Outline platelets.
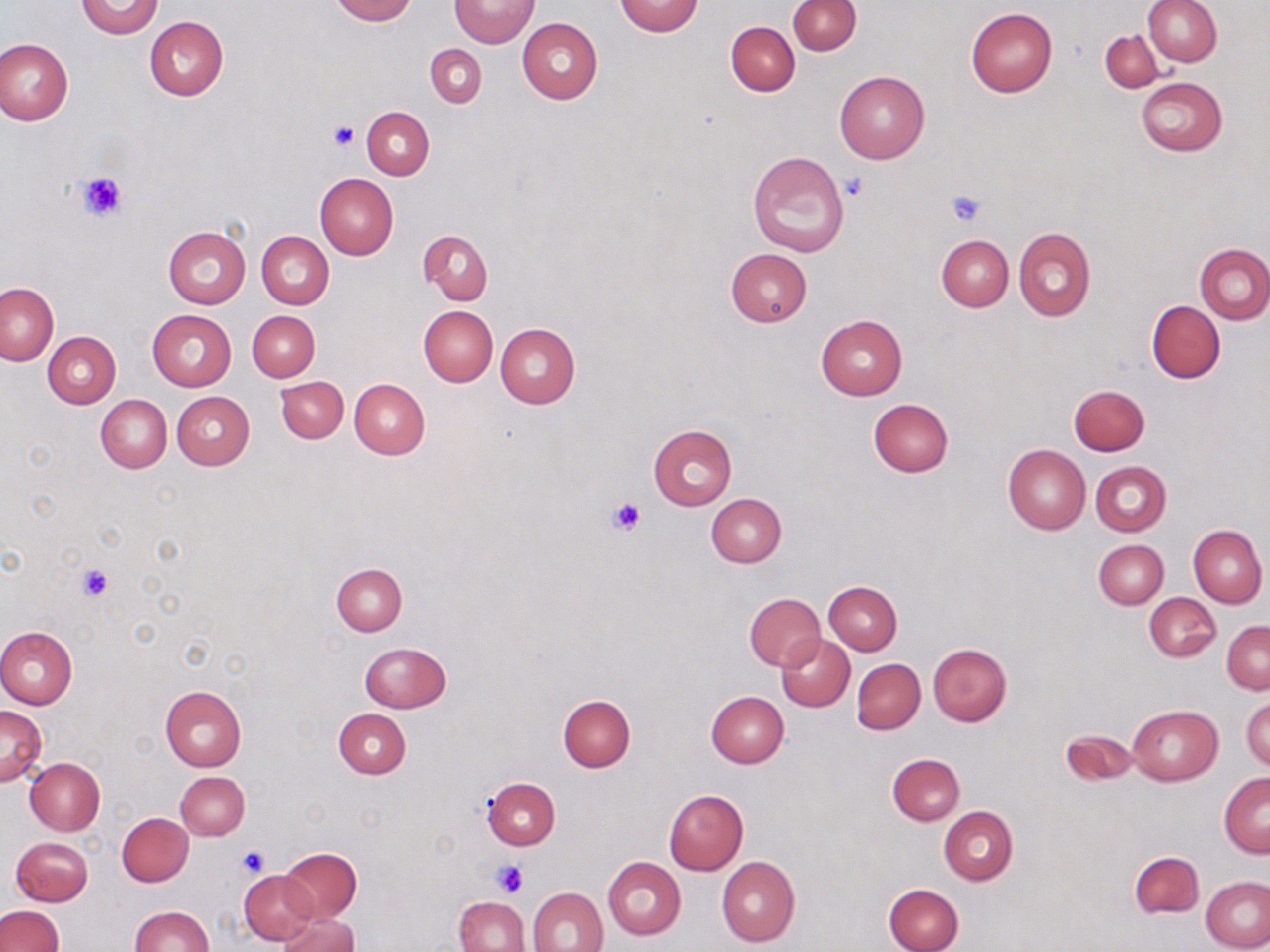
Approximate bounding boxes as named x1/y1/x2/y2 corners in pixels.
Platelets: (x1=329, y1=121, x2=359, y2=151), (x1=75, y1=170, x2=129, y2=222), (x1=842, y1=172, x2=868, y2=201), (x1=945, y1=189, x2=987, y2=226), (x1=609, y1=498, x2=646, y2=535), (x1=75, y1=564, x2=114, y2=601), (x1=234, y1=843, x2=271, y2=878), (x1=490, y1=859, x2=526, y2=898).

Uninfected red blood cell locations: (x1=77, y1=0, x2=163, y2=38), (x1=329, y1=0, x2=417, y2=23), (x1=450, y1=0, x2=538, y2=48), (x1=1143, y1=0, x2=1222, y2=66), (x1=614, y1=1, x2=704, y2=36), (x1=787, y1=1, x2=860, y2=55), (x1=966, y1=8, x2=1058, y2=97), (x1=145, y1=16, x2=228, y2=100), (x1=517, y1=17, x2=603, y2=103), (x1=726, y1=22, x2=799, y2=95), (x1=1100, y1=31, x2=1163, y2=91), (x1=0, y1=38, x2=72, y2=127), (x1=426, y1=44, x2=486, y2=108), (x1=834, y1=70, x2=930, y2=163), (x1=1136, y1=76, x2=1228, y2=156), (x1=361, y1=106, x2=434, y2=180), (x1=746, y1=150, x2=849, y2=256), (x1=315, y1=173, x2=399, y2=259), (x1=163, y1=226, x2=251, y2=309), (x1=1013, y1=227, x2=1095, y2=322), (x1=418, y1=230, x2=493, y2=304), (x1=257, y1=231, x2=334, y2=309), (x1=937, y1=236, x2=1013, y2=311), (x1=1196, y1=243, x2=1270, y2=324), (x1=725, y1=248, x2=811, y2=327), (x1=1169, y1=254, x2=1264, y2=358), (x1=0, y1=282, x2=59, y2=366), (x1=1146, y1=300, x2=1225, y2=383), (x1=418, y1=306, x2=496, y2=386), (x1=147, y1=310, x2=235, y2=392), (x1=247, y1=311, x2=319, y2=380), (x1=816, y1=315, x2=907, y2=400), (x1=494, y1=323, x2=579, y2=408), (x1=43, y1=332, x2=120, y2=408), (x1=276, y1=376, x2=348, y2=442), (x1=349, y1=378, x2=430, y2=459), (x1=1069, y1=385, x2=1149, y2=456), (x1=172, y1=392, x2=254, y2=470), (x1=96, y1=395, x2=171, y2=472), (x1=867, y1=398, x2=954, y2=477), (x1=647, y1=424, x2=738, y2=510), (x1=1003, y1=443, x2=1090, y2=534), (x1=1092, y1=461, x2=1171, y2=536), (x1=706, y1=494, x2=786, y2=567), (x1=1188, y1=525, x2=1267, y2=608), (x1=1093, y1=539, x2=1168, y2=609), (x1=331, y1=563, x2=407, y2=635), (x1=824, y1=581, x2=902, y2=655), (x1=743, y1=593, x2=825, y2=671), (x1=1145, y1=593, x2=1220, y2=661), (x1=1223, y1=620, x2=1269, y2=694), (x1=0, y1=626, x2=77, y2=709), (x1=776, y1=634, x2=854, y2=711), (x1=359, y1=642, x2=451, y2=713), (x1=927, y1=643, x2=1012, y2=726), (x1=852, y1=658, x2=925, y2=734), (x1=160, y1=685, x2=246, y2=771), (x1=707, y1=690, x2=789, y2=767), (x1=1241, y1=693, x2=1269, y2=771), (x1=558, y1=695, x2=635, y2=772), (x1=1127, y1=704, x2=1222, y2=786), (x1=0, y1=706, x2=47, y2=786), (x1=333, y1=708, x2=410, y2=778), (x1=1060, y1=728, x2=1137, y2=787), (x1=888, y1=753, x2=964, y2=824), (x1=25, y1=757, x2=105, y2=835), (x1=175, y1=772, x2=249, y2=840), (x1=1219, y1=773, x2=1270, y2=858), (x1=482, y1=778, x2=560, y2=849), (x1=663, y1=790, x2=747, y2=874), (x1=939, y1=806, x2=1018, y2=885), (x1=117, y1=813, x2=193, y2=887), (x1=12, y1=836, x2=93, y2=906), (x1=279, y1=847, x2=361, y2=922), (x1=1129, y1=851, x2=1204, y2=919), (x1=603, y1=856, x2=686, y2=939), (x1=717, y1=857, x2=800, y2=947), (x1=239, y1=869, x2=319, y2=945), (x1=1201, y1=875, x2=1270, y2=951), (x1=884, y1=882, x2=963, y2=951), (x1=528, y1=886, x2=608, y2=952), (x1=454, y1=896, x2=527, y2=952), (x1=0, y1=905, x2=65, y2=952), (x1=129, y1=906, x2=212, y2=952), (x1=277, y1=912, x2=358, y2=952). Slide-level diagnosis: negative for blood parasites. Image is 1270×952 pixels. Light microscopy. May-Grünwald-Giemsa stain. Captured at 1000x magnification. Thin blood film. Single field of view.